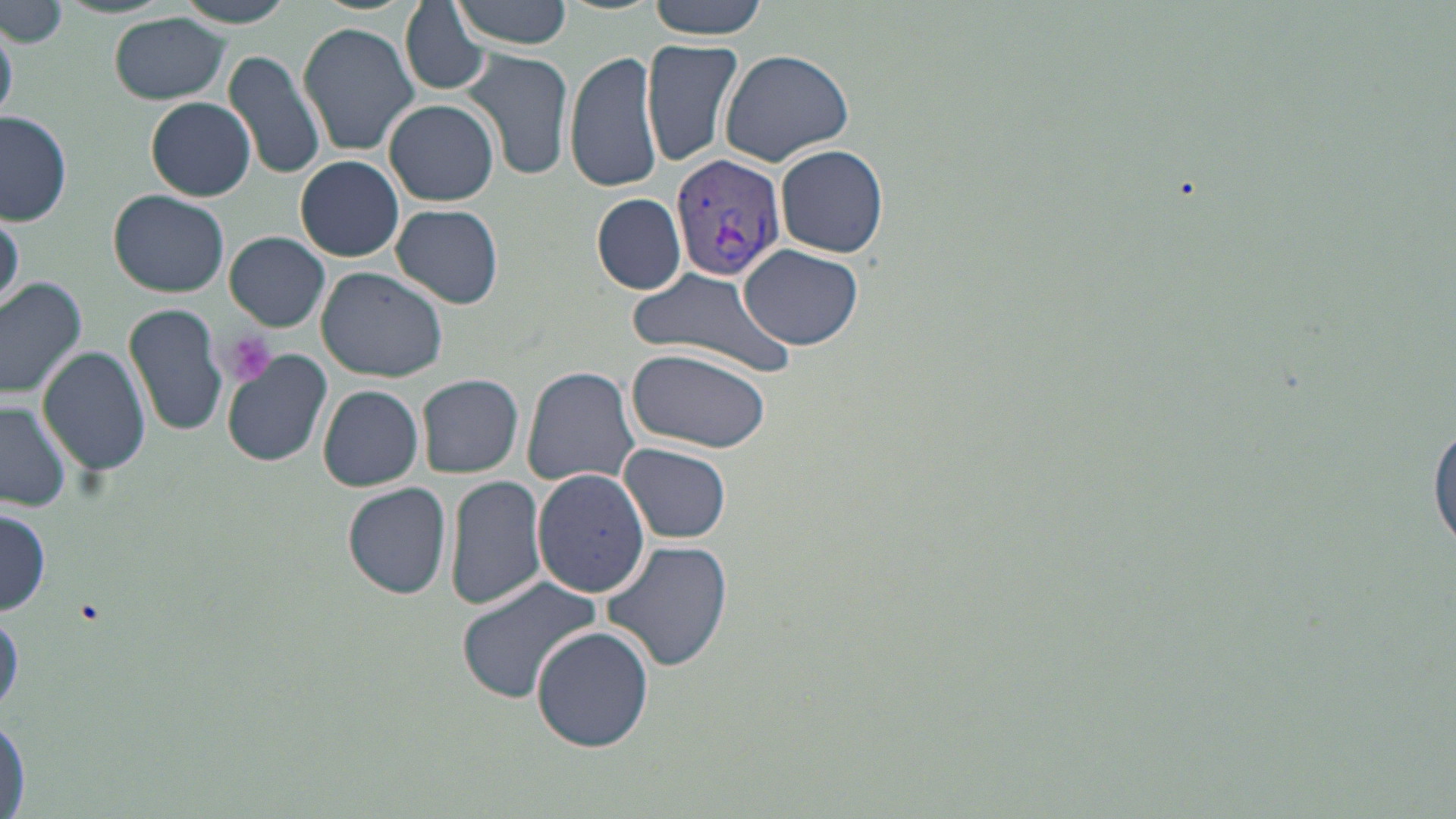
Approximate bounding boxes as named x1/y1/x2/y2 corners in pixels. Plasmodium vivax-infected red blood cell locations: (x1=667, y1=151, x2=787, y2=284). Platelet locations: (x1=217, y1=329, x2=280, y2=390). Uninfected red blood cell locations: (x1=645, y1=0, x2=771, y2=39), (x1=1, y1=1, x2=69, y2=47), (x1=450, y1=1, x2=575, y2=49), (x1=397, y1=2, x2=491, y2=94), (x1=0, y1=14, x2=18, y2=124), (x1=111, y1=14, x2=228, y2=105), (x1=298, y1=22, x2=418, y2=156), (x1=642, y1=37, x2=746, y2=169), (x1=461, y1=48, x2=575, y2=183), (x1=719, y1=48, x2=855, y2=168), (x1=224, y1=49, x2=325, y2=182), (x1=564, y1=49, x2=664, y2=193), (x1=146, y1=97, x2=257, y2=201), (x1=385, y1=99, x2=500, y2=205), (x1=1, y1=111, x2=71, y2=226), (x1=775, y1=143, x2=890, y2=258), (x1=295, y1=155, x2=404, y2=261), (x1=109, y1=189, x2=229, y2=296), (x1=592, y1=194, x2=686, y2=295), (x1=389, y1=203, x2=505, y2=308), (x1=1, y1=210, x2=22, y2=313), (x1=225, y1=233, x2=330, y2=330), (x1=739, y1=244, x2=864, y2=350), (x1=316, y1=265, x2=448, y2=382), (x1=626, y1=267, x2=794, y2=373), (x1=0, y1=276, x2=88, y2=401), (x1=123, y1=303, x2=229, y2=439), (x1=38, y1=346, x2=151, y2=475), (x1=624, y1=346, x2=772, y2=454), (x1=223, y1=352, x2=332, y2=468), (x1=521, y1=365, x2=642, y2=487), (x1=418, y1=374, x2=523, y2=478), (x1=316, y1=383, x2=424, y2=491), (x1=0, y1=400, x2=75, y2=513), (x1=1428, y1=410, x2=1456, y2=562), (x1=618, y1=442, x2=732, y2=544), (x1=531, y1=465, x2=653, y2=598), (x1=445, y1=474, x2=548, y2=610), (x1=342, y1=481, x2=454, y2=602), (x1=0, y1=508, x2=52, y2=619), (x1=600, y1=538, x2=734, y2=670), (x1=455, y1=576, x2=604, y2=704), (x1=0, y1=608, x2=22, y2=719), (x1=531, y1=626, x2=658, y2=753), (x1=0, y1=717, x2=28, y2=814). Slide-level diagnosis: Plasmodium vivax. Single field of view. Image is 1456×819 pixels. Light microscopy. Thin blood smear. 1000x magnification. May-Grünwald-Giemsa-stained preparation.